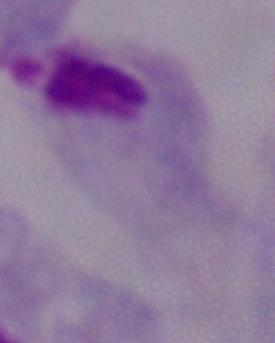

Summary:
  - Magnification: 1000x
  - Identification: trichomonad
  - Modality: photomicrograph